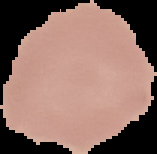
image_type: cell region segmented out of the field of view; surrounding area masked to black
image_size: 157×154 pixels
result: no Plasmodium parasites detected
preparation: thin blood smear